Assess this cell for malaria.
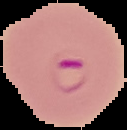
Parasitized.

Image is 127×130 pixels. Segmented cell region on a black background. From a thin blood film.